Classify this cell by malaria status.
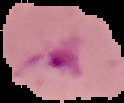

It is parasitized.

image type = segmented cell region on a black background
preparation = thin blood film
image size = 124×103 pixels